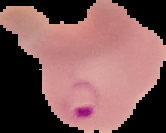
Summary:
  - Image size: 166×133 pixels
  - Result: Plasmodium parasites detected
  - Image type: segmented cell region with the area outside set to black
  - Preparation: thin blood film